Locate every uninfected red blood cell.
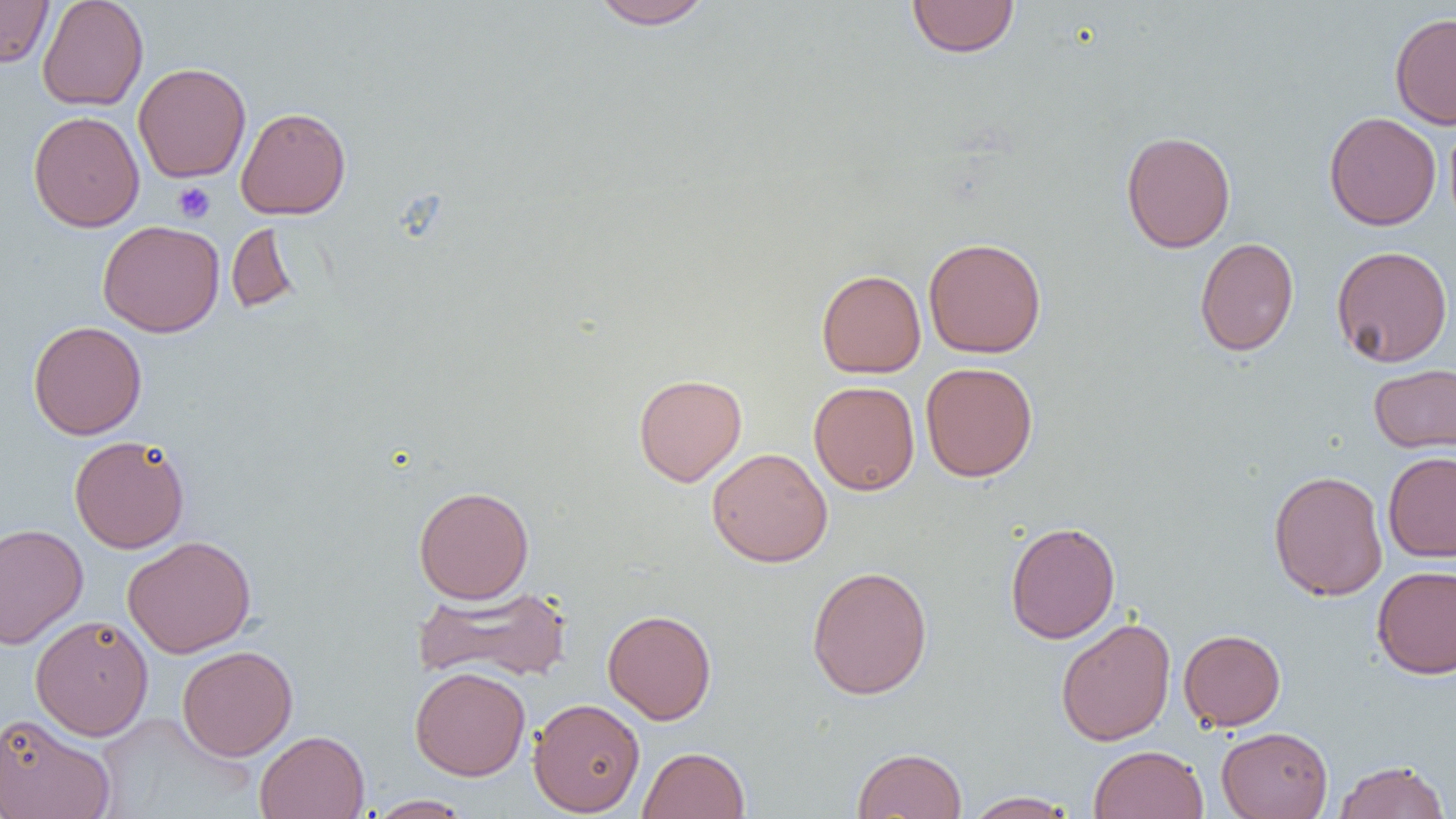
Approximate bounding boxes as named x1/y1/x2/y2 corners in pixels.
Uninfected red blood cells: (x1=0, y1=0, x2=53, y2=67), (x1=37, y1=0, x2=148, y2=111), (x1=589, y1=0, x2=715, y2=30), (x1=906, y1=0, x2=1019, y2=58), (x1=1389, y1=12, x2=1456, y2=129), (x1=133, y1=62, x2=251, y2=183), (x1=236, y1=106, x2=351, y2=219), (x1=28, y1=110, x2=145, y2=232), (x1=1323, y1=112, x2=1441, y2=231), (x1=1120, y1=130, x2=1236, y2=253), (x1=97, y1=220, x2=224, y2=337), (x1=226, y1=221, x2=300, y2=314), (x1=923, y1=237, x2=1047, y2=359), (x1=1194, y1=237, x2=1299, y2=357), (x1=1331, y1=245, x2=1453, y2=367), (x1=816, y1=269, x2=926, y2=378), (x1=28, y1=321, x2=147, y2=440), (x1=920, y1=362, x2=1038, y2=482), (x1=1368, y1=363, x2=1456, y2=454), (x1=633, y1=373, x2=747, y2=487), (x1=808, y1=381, x2=920, y2=495), (x1=69, y1=434, x2=190, y2=553), (x1=706, y1=447, x2=832, y2=567), (x1=1383, y1=451, x2=1456, y2=563), (x1=1268, y1=470, x2=1388, y2=601), (x1=413, y1=485, x2=534, y2=604), (x1=1005, y1=521, x2=1121, y2=644), (x1=0, y1=523, x2=88, y2=649), (x1=122, y1=535, x2=256, y2=658), (x1=806, y1=566, x2=933, y2=699), (x1=1372, y1=566, x2=1456, y2=679), (x1=412, y1=585, x2=573, y2=684), (x1=602, y1=609, x2=717, y2=724), (x1=30, y1=615, x2=154, y2=740), (x1=1056, y1=617, x2=1176, y2=746), (x1=1178, y1=629, x2=1286, y2=730), (x1=177, y1=645, x2=298, y2=760), (x1=410, y1=666, x2=530, y2=781), (x1=137, y1=674, x2=283, y2=783), (x1=528, y1=697, x2=645, y2=816), (x1=93, y1=711, x2=257, y2=817), (x1=0, y1=712, x2=116, y2=819), (x1=1217, y1=726, x2=1333, y2=819), (x1=255, y1=730, x2=370, y2=819), (x1=1089, y1=745, x2=1209, y2=819), (x1=638, y1=746, x2=751, y2=819), (x1=852, y1=747, x2=967, y2=818), (x1=1333, y1=759, x2=1450, y2=819), (x1=964, y1=791, x2=1079, y2=818), (x1=366, y1=794, x2=474, y2=818).

Platelet locations: (x1=172, y1=181, x2=215, y2=223). Slide-level diagnosis: no evidence of blood parasites. Image is 1456×819 pixels. Single field of view. Thin blood film. 1000x magnification. Light microscopy.